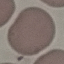

Summary:
  - Malaria status: uninfected
  - Capture: smartphone through the microscope eyepiece
  - Stain: Giemsa
  - Image type: automatically extracted cell patch, resized to 64 × 64 pixels
  - Preparation: thin blood film